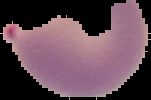
image size = 151×100 pixels
image type = segmented cell region with the area outside set to black
preparation = thin blood smear
malaria status = parasitized